State the blood parasite species.
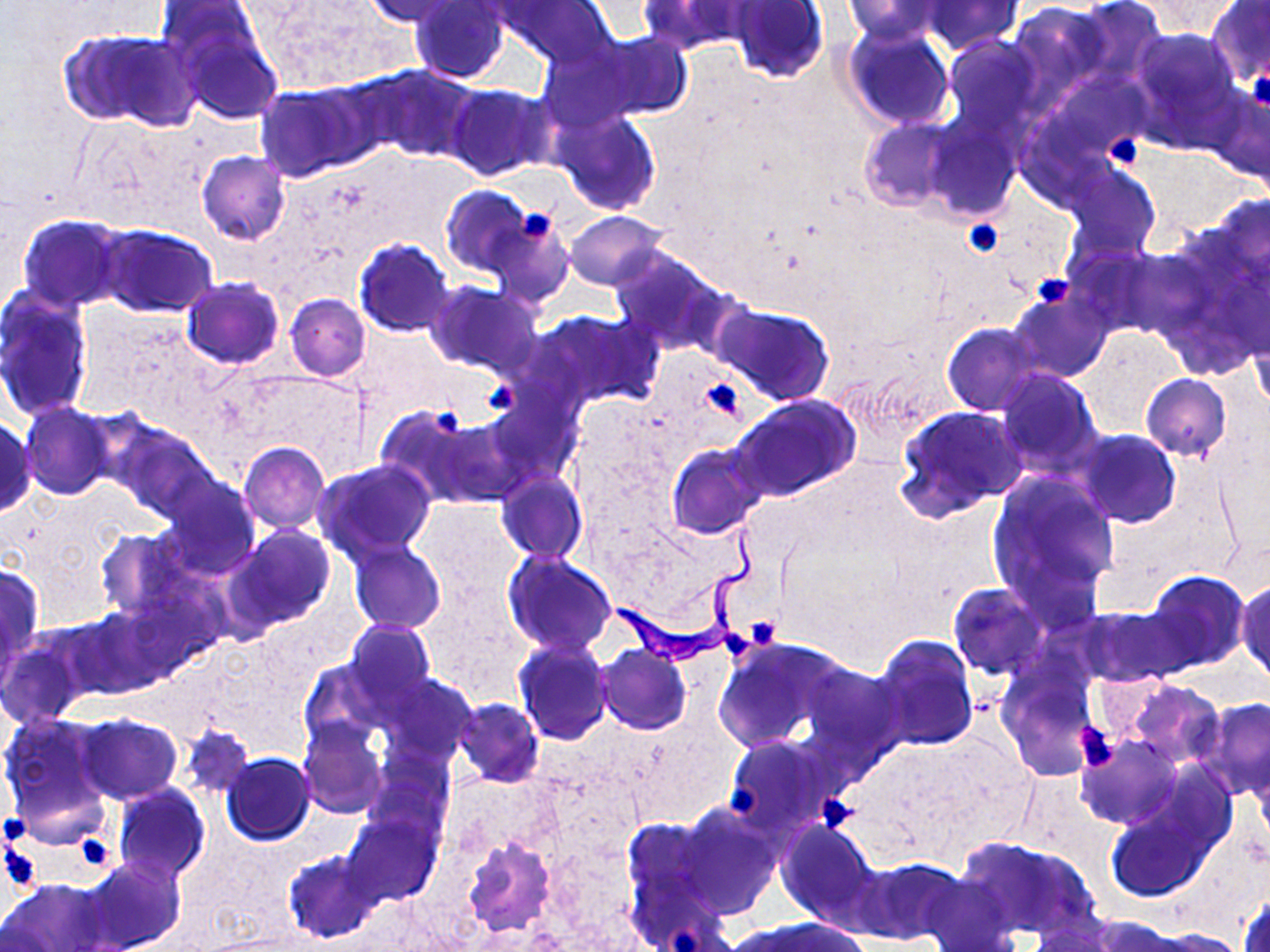
Trypanosoma brucei.

Approximate bounding boxes as (x1,y1)-(x2,y2) corner pairs in pixels. Platelet locations: (1248,68)-(1270,110), (1104,134)-(1144,170), (516,210)-(558,244), (962,218)-(1003,258), (1033,272)-(1075,311), (698,379)-(745,421), (483,382)-(518,415), (434,407)-(463,438), (750,619)-(777,645), (723,634)-(753,661), (1078,725)-(1117,772), (728,780)-(759,818), (815,793)-(855,832), (2,812)-(34,843), (78,839)-(110,864), (1,845)-(41,892), (670,924)-(706,950). Uninfected red blood cell locations: (506,0)-(615,67), (1073,0)-(1166,87), (363,1)-(472,27), (410,1)-(512,85), (638,1)-(753,54), (730,1)-(828,84), (841,1)-(948,44), (921,1)-(1024,54), (1143,1)-(1241,37), (153,2)-(269,75), (1208,2)-(1270,84), (1009,3)-(1106,97), (842,24)-(954,129), (174,25)-(282,124), (1128,27)-(1243,136), (69,31)-(199,130), (589,32)-(693,122), (942,34)-(1044,135), (534,37)-(646,132), (369,66)-(479,162), (1046,69)-(1148,161), (307,76)-(405,166), (446,84)-(553,181), (1205,84)-(1270,184), (255,86)-(358,182), (551,108)-(661,215), (859,119)-(958,211), (924,121)-(1019,220), (196,150)-(290,244), (1061,161)-(1161,260), (441,185)-(531,277), (564,210)-(668,290), (486,211)-(574,309), (18,215)-(128,311), (96,225)-(218,318), (354,238)-(454,338), (609,245)-(728,354), (180,277)-(285,369), (425,280)-(540,376), (0,286)-(94,422), (1007,289)-(1111,382), (285,294)-(371,382), (715,303)-(834,406), (529,309)-(662,411), (1247,315)-(1269,414), (943,323)-(1042,416), (994,369)-(1103,478), (1141,374)-(1231,461), (482,391)-(583,493), (732,395)-(860,501), (20,402)-(119,500), (376,404)-(484,506), (894,405)-(1027,520), (433,412)-(530,506), (0,417)-(38,518), (106,420)-(217,521), (1076,429)-(1181,527), (238,442)-(329,532), (667,444)-(765,539), (312,459)-(438,564), (496,472)-(587,565), (986,473)-(1120,609), (158,474)-(261,580), (413,502)-(519,602), (230,525)-(336,629), (96,528)-(190,621), (348,540)-(446,634), (503,552)-(617,657), (0,563)-(43,661), (1147,572)-(1249,671), (1236,580)-(1269,683), (947,582)-(1050,680), (1079,605)-(1185,687), (65,608)-(165,698), (344,621)-(436,709), (872,635)-(978,751), (0,638)-(84,728), (513,638)-(612,746), (713,638)-(848,756), (596,645)-(691,734), (298,659)-(387,751), (796,662)-(907,769), (998,664)-(1101,780), (377,668)-(495,764), (1125,680)-(1225,769), (1195,697)-(1270,799), (454,698)-(544,789), (0,714)-(113,835), (76,715)-(182,804), (299,722)-(388,820), (179,724)-(254,799), (1076,733)-(1180,829), (723,735)-(840,838), (1091,745)-(1209,869), (221,752)-(315,844), (365,752)-(452,843), (112,784)-(210,885), (1104,792)-(1227,902), (672,805)-(783,918), (343,810)-(441,907), (622,817)-(719,919), (776,819)-(882,929), (461,835)-(560,935), (956,836)-(1099,942), (285,851)-(381,942), (81,855)-(185,952), (856,857)-(966,946), (918,874)-(1020,952), (1,877)-(111,952), (1237,886)-(1269,952), (1081,915)-(1184,952), (740,917)-(868,952), (1022,925)-(1125,951), (1145,928)-(1249,952). Trypanosoma brucei locations: (612,528)-(765,666). One field of a larger specimen. Light microscopy. Image is 1270×952 pixels. 1000x magnification. May-Grünwald-Giemsa-stained preparation. Thin blood smear.